Identify the parasite.
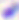
Toxoplasma gondii.

Summary:
  - Magnification: 400x
  - Modality: photomicrograph